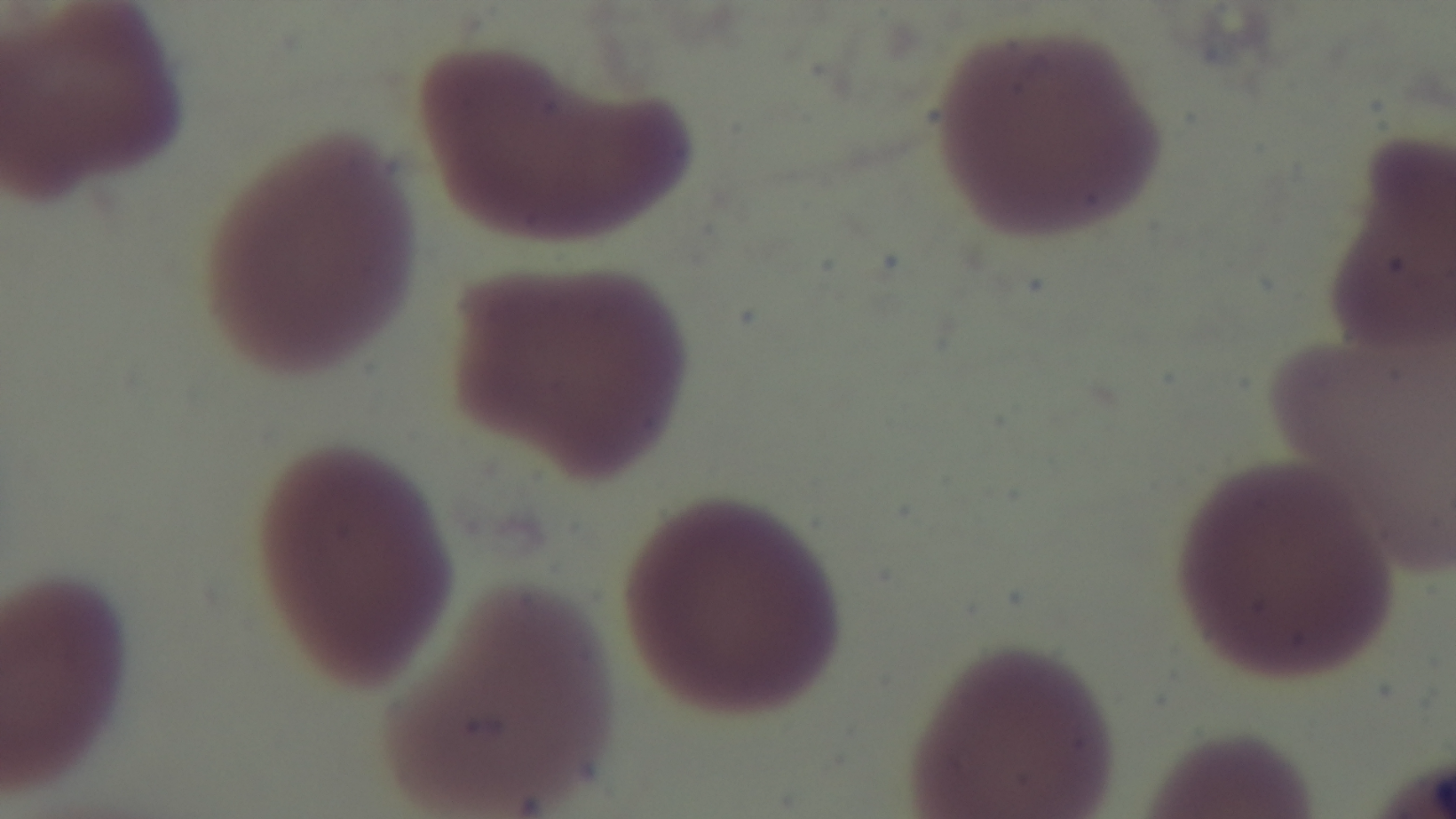
100x oil-immersion objective. Malaria status: negative. Captured with a mounted 4K digital camera. Giemsa stain. Single field of view. Preparation: thin smear. Photomicrograph.